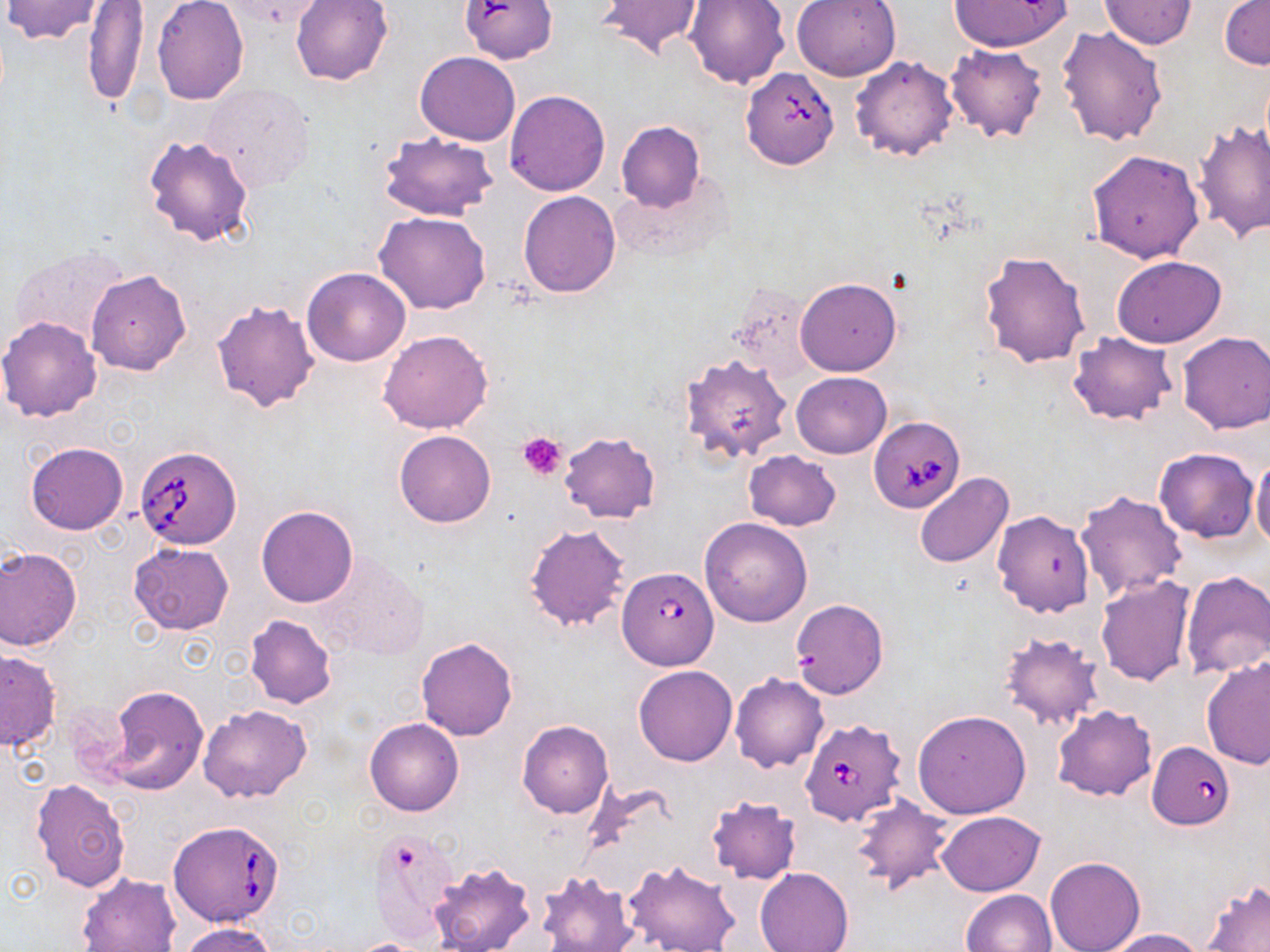

slide_level_diagnosis: Babesia divergens
stain: May-Grünwald-Giemsa
babesia_divergens_infected_red_blood_cell_locations: 'approximate bounding boxes as named x1/y1/x2/y2 corners in pixels: (x1=740, y1=66, x2=840, y2=170), (x1=869, y1=417, x2=963, y2=513), (x1=134, y1=444, x2=243, y2=549), (x1=616, y1=565, x2=719, y2=670), (x1=799, y1=716, x2=906, y2=827), (x1=1148, y1=740, x2=1236, y2=829), (x1=167, y1=820, x2=286, y2=928)'
uninfected_red_blood_cell_locations: 'approximate bounding boxes as named x1/y1/x2/y2 corners in pixels: (x1=218, y1=0, x2=328, y2=30), (x1=291, y1=0, x2=393, y2=86), (x1=596, y1=0, x2=706, y2=60), (x1=686, y1=0, x2=789, y2=88), (x1=791, y1=0, x2=901, y2=81), (x1=948, y1=0, x2=1068, y2=53), (x1=2, y1=1, x2=106, y2=43), (x1=1100, y1=1, x2=1197, y2=49), (x1=1220, y1=1, x2=1270, y2=71), (x1=81, y1=2, x2=149, y2=107), (x1=152, y1=2, x2=248, y2=105), (x1=459, y1=2, x2=563, y2=68), (x1=1057, y1=26, x2=1168, y2=147), (x1=944, y1=44, x2=1048, y2=142), (x1=416, y1=51, x2=520, y2=145), (x1=849, y1=54, x2=960, y2=162), (x1=200, y1=82, x2=316, y2=192), (x1=504, y1=89, x2=610, y2=196), (x1=1193, y1=119, x2=1270, y2=242), (x1=616, y1=121, x2=706, y2=211), (x1=378, y1=131, x2=498, y2=222), (x1=143, y1=134, x2=255, y2=247), (x1=1087, y1=149, x2=1204, y2=262), (x1=518, y1=190, x2=621, y2=297), (x1=374, y1=211, x2=493, y2=314), (x1=8, y1=246, x2=133, y2=353), (x1=980, y1=250, x2=1091, y2=368), (x1=1112, y1=255, x2=1227, y2=347), (x1=301, y1=267, x2=412, y2=367), (x1=87, y1=269, x2=191, y2=375), (x1=795, y1=277, x2=901, y2=377), (x1=727, y1=282, x2=815, y2=381), (x1=211, y1=299, x2=321, y2=413), (x1=1, y1=316, x2=103, y2=422), (x1=378, y1=329, x2=493, y2=434), (x1=1177, y1=331, x2=1270, y2=434), (x1=1067, y1=332, x2=1178, y2=425), (x1=679, y1=353, x2=792, y2=464), (x1=792, y1=372, x2=891, y2=458), (x1=394, y1=429, x2=497, y2=528), (x1=559, y1=432, x2=661, y2=522), (x1=24, y1=441, x2=128, y2=535), (x1=1154, y1=447, x2=1259, y2=542), (x1=744, y1=450, x2=841, y2=531), (x1=1249, y1=451, x2=1270, y2=551), (x1=913, y1=472, x2=1014, y2=568), (x1=1075, y1=490, x2=1189, y2=599), (x1=256, y1=505, x2=359, y2=608), (x1=992, y1=510, x2=1095, y2=618), (x1=699, y1=517, x2=813, y2=627), (x1=523, y1=523, x2=633, y2=633), (x1=128, y1=543, x2=233, y2=635), (x1=0, y1=546, x2=83, y2=650), (x1=312, y1=551, x2=428, y2=661), (x1=1180, y1=571, x2=1270, y2=679), (x1=1095, y1=575, x2=1197, y2=685), (x1=789, y1=598, x2=890, y2=699), (x1=244, y1=614, x2=339, y2=709), (x1=998, y1=631, x2=1104, y2=731), (x1=415, y1=637, x2=519, y2=741), (x1=0, y1=648, x2=61, y2=750), (x1=1201, y1=656, x2=1270, y2=769), (x1=633, y1=665, x2=737, y2=766), (x1=730, y1=673, x2=829, y2=773), (x1=103, y1=684, x2=208, y2=795), (x1=199, y1=704, x2=312, y2=804), (x1=1051, y1=704, x2=1157, y2=802), (x1=913, y1=710, x2=1031, y2=819), (x1=365, y1=717, x2=464, y2=816), (x1=517, y1=719, x2=614, y2=819), (x1=30, y1=778, x2=131, y2=893), (x1=705, y1=795, x2=802, y2=885), (x1=850, y1=796, x2=953, y2=895), (x1=937, y1=810, x2=1046, y2=895), (x1=371, y1=830, x2=459, y2=944), (x1=1045, y1=856, x2=1145, y2=952), (x1=624, y1=859, x2=740, y2=952), (x1=428, y1=861, x2=537, y2=952), (x1=755, y1=866, x2=854, y2=952), (x1=537, y1=871, x2=638, y2=952), (x1=76, y1=873, x2=179, y2=952), (x1=1202, y1=882, x2=1270, y2=952), (x1=961, y1=889, x2=1057, y2=952), (x1=179, y1=923, x2=281, y2=952), (x1=1102, y1=928, x2=1205, y2=951), (x1=346, y1=938, x2=441, y2=952)'
image_size: 1270×952 pixels
preparation: thin blood film
platelet_locations: 'approximate bounding boxes as named x1/y1/x2/y2 corners in pixels: (x1=518, y1=431, x2=568, y2=479)'
field_of_view: one of a larger specimen
modality: light microscopy
magnification: 1000x